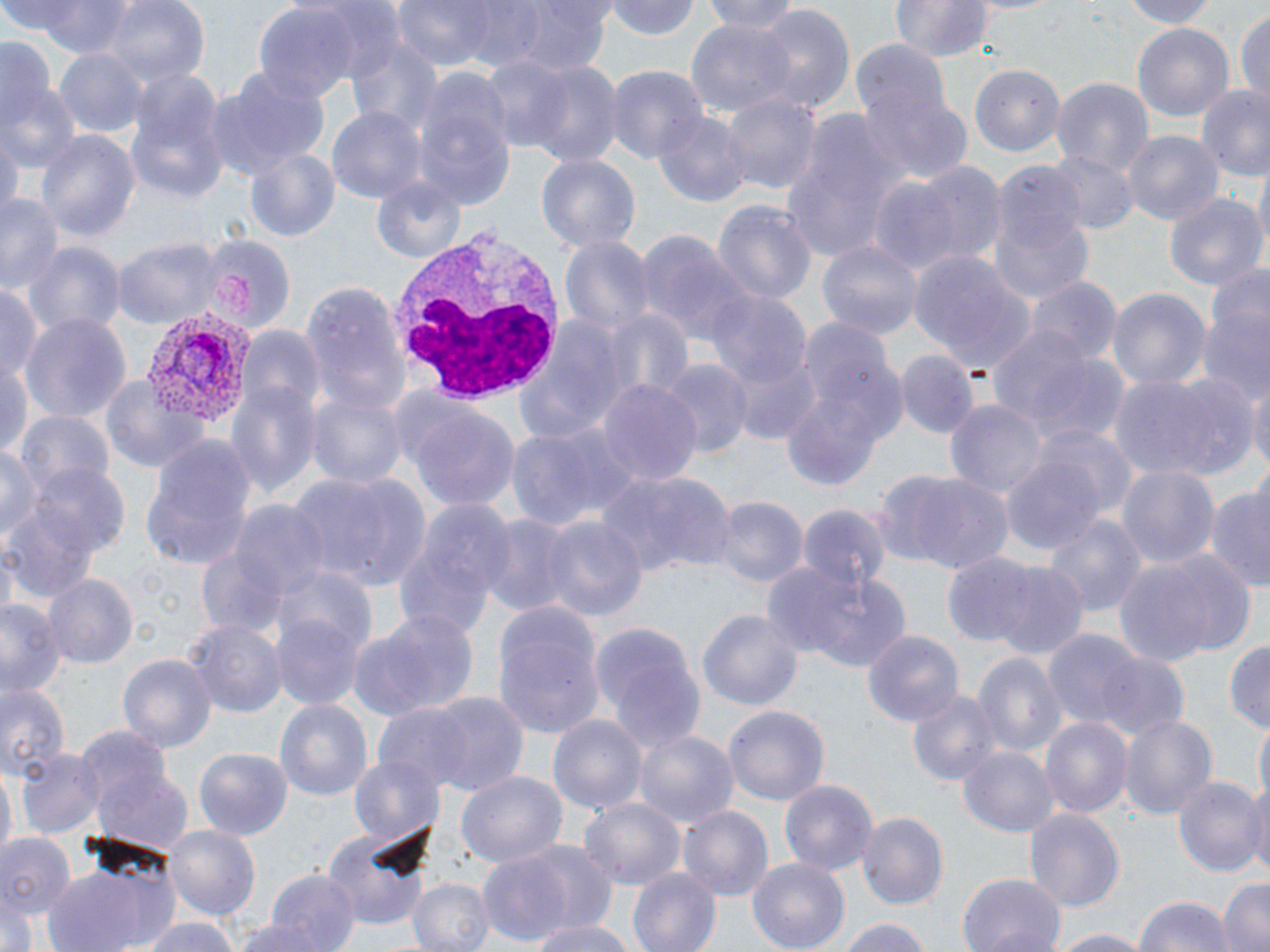
slide-level diagnosis = Plasmodium vivax
modality = optical microscopy
image size = 1270×952 pixels
field of view = one of a larger specimen
stain = May-Grünwald-Giemsa
Plasmodium vivax-infected red blood cell locations = approximate bounding boxes as (x1,y1)-(x2,y2) corner pairs in pixels: (143,311)-(258,427)
magnification = 1000x
white blood cell locations = approximate bounding boxes as (x1,y1)-(x2,y2) corner pairs in pixels: (387,222)-(565,404)
platelet locations = approximate bounding boxes as (x1,y1)-(x2,y2) corner pairs in pixels: (214,273)-(257,311)
uninfected red blood cell locations = approximate bounding boxes as (x1,y1)-(x2,y2) corner pairs in pixels: (14,0)-(135,56), (386,0)-(515,75), (507,0)-(616,74), (607,0)-(703,40), (698,0)-(808,30), (890,0)-(995,61), (1111,0)-(1224,27), (100,1)-(210,92), (253,4)-(361,107), (751,6)-(856,118), (1234,6)-(1270,105), (685,18)-(797,123), (1132,22)-(1235,129), (845,32)-(959,138), (0,34)-(58,128), (346,36)-(442,134), (54,46)-(148,137), (481,54)-(580,155), (519,59)-(623,166), (969,61)-(1066,157), (605,67)-(704,164), (205,68)-(330,177), (123,70)-(230,205), (1052,76)-(1153,178), (411,77)-(515,208), (0,83)-(80,176), (1196,87)-(1270,183), (720,88)-(820,195), (857,91)-(972,188), (326,105)-(425,208), (652,108)-(751,210), (778,108)-(905,261), (35,129)-(139,247), (1119,130)-(1224,228), (243,146)-(340,243), (1048,150)-(1136,233), (536,154)-(639,254), (1252,155)-(1269,265), (912,162)-(1007,268), (369,174)-(468,264), (988,174)-(1093,306), (866,178)-(963,277), (1163,191)-(1267,292), (0,194)-(64,295), (713,199)-(816,310), (635,228)-(758,350), (560,232)-(654,339), (111,235)-(221,331), (196,239)-(290,335), (818,240)-(922,341), (22,241)-(123,337), (909,251)-(1037,378), (1028,274)-(1120,367), (300,280)-(407,415), (0,282)-(43,394), (1107,287)-(1213,392), (706,292)-(811,396), (1196,309)-(1270,403), (519,310)-(633,444), (599,310)-(693,409), (18,313)-(130,425), (779,322)-(909,486), (986,327)-(1124,451), (236,329)-(323,422), (726,344)-(822,445), (897,351)-(977,437), (0,357)-(32,456), (660,358)-(752,462), (100,373)-(208,473), (1106,373)-(1244,483), (227,375)-(321,499), (1247,376)-(1270,478), (595,379)-(704,490), (305,384)-(408,493), (945,397)-(1047,501), (403,401)-(523,516), (15,410)-(115,497), (507,422)-(636,531), (1037,425)-(1138,520), (139,437)-(258,570), (2,444)-(44,554), (998,448)-(1111,560), (15,462)-(133,572), (1116,464)-(1220,575), (596,470)-(737,579), (881,470)-(1017,576), (289,472)-(435,591), (1204,487)-(1270,586), (714,495)-(806,587), (391,499)-(515,638), (192,501)-(328,639), (798,502)-(892,595), (1043,512)-(1146,619), (477,513)-(579,619), (537,514)-(646,625), (1115,550)-(1252,664), (941,552)-(1044,647), (771,562)-(912,671), (991,562)-(1090,661), (272,566)-(379,662), (45,573)-(137,668), (0,597)-(64,699), (490,598)-(607,741), (699,608)-(802,715), (351,609)-(479,721), (270,611)-(365,711), (184,619)-(285,717), (588,619)-(705,752), (863,629)-(963,728), (1045,630)-(1147,730), (1226,638)-(1269,731), (1085,648)-(1192,742), (119,651)-(216,751), (972,651)-(1066,761), (0,679)-(69,779), (905,686)-(1002,788), (424,692)-(529,797), (273,696)-(374,800), (724,703)-(829,809), (372,705)-(475,799), (548,712)-(647,819), (1118,712)-(1217,822), (1040,715)-(1134,821), (1256,717)-(1269,808), (634,730)-(737,831), (959,744)-(1057,838), (82,746)-(195,854), (15,748)-(102,838), (197,748)-(292,839), (348,752)-(443,851), (0,765)-(15,867), (456,770)-(567,869), (1172,774)-(1265,876), (778,777)-(880,876), (1242,781)-(1270,882), (579,797)-(685,891), (677,804)-(773,904), (1024,806)-(1125,913), (857,812)-(947,908), (167,826)-(260,918), (322,826)-(431,932), (0,833)-(76,923), (511,840)-(620,934), (478,852)-(575,945), (746,856)-(851,951), (40,859)-(185,952), (629,867)-(720,951), (263,869)-(360,952), (957,873)-(1066,952), (405,877)-(493,952), (523,877)-(631,951), (1216,878)-(1270,952), (1132,894)-(1236,952), (229,916)-(336,952), (527,916)-(631,952), (835,916)-(932,952), (134,917)-(244,952), (1048,929)-(1150,952)
preparation = thin blood film